Comment on the morphology of the erythrocytes.
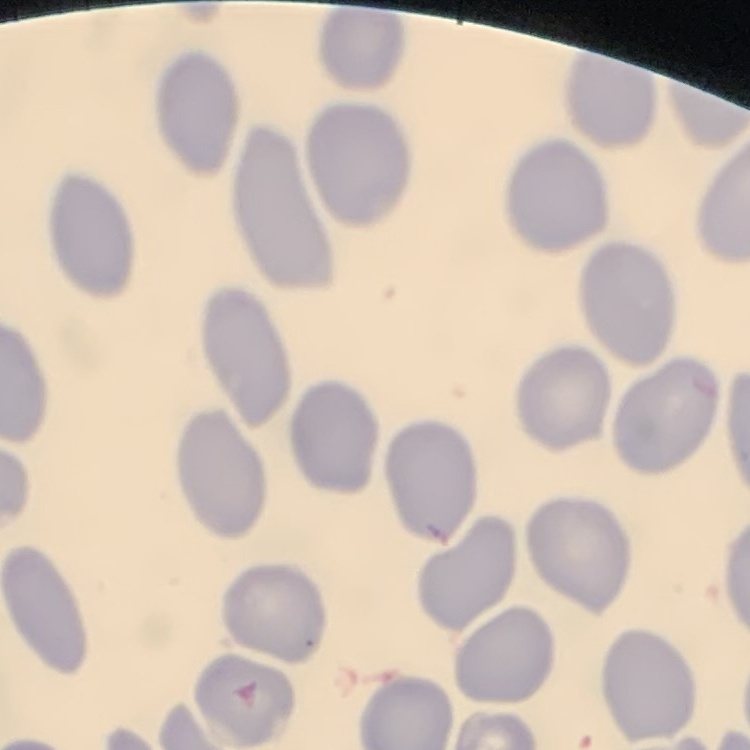
They show no rouleaux formation.

Field's or Giemsa stain. Thin blood film. Square crop of a larger photomicrograph.